Locate and identify every blood parasite.
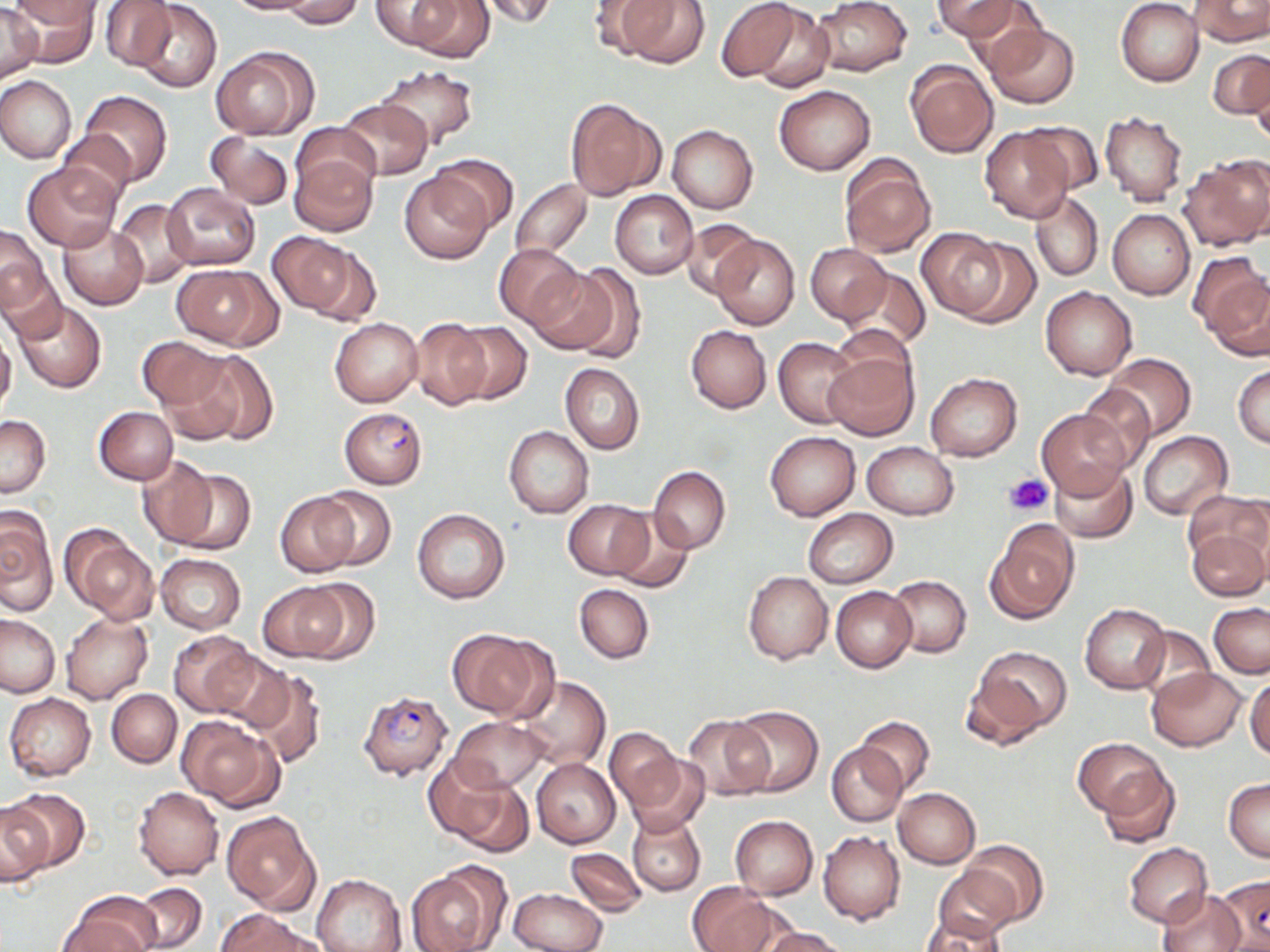

Approximate bounding boxes as (x1,y1)-(x2,y2) corner pairs in pixels.
Plasmodium falciparum-infected red blood cells: (338,407)-(428,489), (357,690)-(454,781), (1214,875)-(1270,951).
No Plasmodium ovale, Plasmodium malariae, Plasmodium vivax, Babesia divergens, or Trypanosoma brucei observed.

slide-level diagnosis = Plasmodium falciparum
magnification = 1000x
image size = 1270×952 pixels
field of view = single
preparation = thin blood film
uninfected red blood cell locations = approximate bounding boxes as (x1,y1)-(x2,y2) corner pairs in pixels: (8,0)-(102,52), (224,0)-(322,16), (280,0)-(366,29), (371,0)-(467,52), (474,0)-(561,27), (586,0)-(670,55), (618,0)-(710,69), (716,0)-(808,85), (812,0)-(911,77), (931,0)-(1026,43), (1116,0)-(1205,86), (1190,0)-(1269,46), (405,1)-(495,63), (100,2)-(176,70), (0,3)-(43,82), (135,3)-(221,91), (749,5)-(836,93), (983,22)-(1078,107), (210,47)-(318,139), (1209,48)-(1270,119), (905,59)-(998,157), (377,64)-(478,149), (0,76)-(76,163), (774,84)-(875,175), (78,90)-(171,186), (564,97)-(664,202), (338,99)-(432,180), (1099,110)-(1189,206), (1015,120)-(1104,196), (293,122)-(379,199), (667,124)-(759,214), (980,126)-(1074,223), (58,130)-(136,204), (205,131)-(294,210), (289,150)-(377,236), (430,154)-(519,233), (839,155)-(936,257), (1181,157)-(1270,252), (22,160)-(123,252), (400,171)-(495,263), (509,179)-(592,261), (162,183)-(260,271), (610,190)-(698,279), (1030,191)-(1104,281), (110,199)-(197,288), (1107,209)-(1195,300), (678,219)-(765,300), (58,224)-(149,309), (1,225)-(54,313), (916,228)-(1009,319), (266,232)-(360,317), (712,233)-(799,330), (950,237)-(1041,327), (302,243)-(384,327), (494,244)-(586,329), (805,245)-(892,324), (1192,253)-(1270,357), (478,257)-(571,368), (1,261)-(68,346), (566,262)-(649,363), (172,265)-(279,349), (838,266)-(931,351), (527,267)-(622,356), (1040,287)-(1137,381), (14,300)-(107,392), (331,318)-(424,407), (410,319)-(491,409), (447,321)-(531,404), (686,325)-(771,413), (0,331)-(16,413), (136,336)-(230,414), (773,337)-(861,429), (823,348)-(916,440), (177,349)-(277,447), (1103,353)-(1196,441), (561,363)-(645,454), (1233,364)-(1270,447), (926,372)-(1021,462), (1078,383)-(1157,474), (95,407)-(178,485), (1037,408)-(1130,501), (0,414)-(50,497), (504,426)-(594,518), (765,431)-(860,520), (1137,431)-(1232,519), (862,442)-(957,519), (136,456)-(220,547), (1050,461)-(1138,543), (648,467)-(730,554), (172,469)-(254,554), (312,487)-(397,571), (276,492)-(359,577), (563,499)-(652,580), (0,507)-(58,613), (412,508)-(509,604), (802,508)-(898,588), (608,510)-(696,592), (988,521)-(1078,622), (1185,522)-(1269,603), (63,529)-(157,622), (154,554)-(246,634), (743,570)-(833,665), (888,575)-(971,657), (298,581)-(379,662), (257,582)-(352,661), (575,583)-(654,664), (832,587)-(916,673), (1080,603)-(1171,694), (1209,603)-(1270,677), (0,613)-(59,697), (61,614)-(152,705), (1136,626)-(1215,702), (448,629)-(547,719), (168,630)-(259,717), (970,646)-(1072,741), (212,652)-(294,737), (1146,667)-(1246,751), (247,669)-(328,769), (1245,675)-(1270,762), (513,676)-(610,770), (107,689)-(181,767), (5,692)-(97,781), (730,706)-(822,795), (683,715)-(774,802), (177,716)-(281,809), (447,716)-(546,793), (855,716)-(935,795), (606,726)-(684,811), (1075,737)-(1169,821), (827,744)-(906,826), (628,754)-(709,835), (1095,756)-(1181,848), (531,758)-(620,848), (445,776)-(533,856), (1224,778)-(1270,862), (133,786)-(224,880), (893,787)-(981,867), (3,788)-(86,875), (0,800)-(49,886), (626,809)-(706,897), (221,811)-(320,914), (729,815)-(818,899), (818,831)-(905,925), (960,839)-(1048,927), (1124,843)-(1213,927), (566,848)-(646,916), (933,865)-(1023,943), (406,867)-(499,952), (312,874)-(406,952), (133,883)-(206,950), (687,883)-(780,952), (510,888)-(606,952), (1155,888)-(1246,952), (59,893)-(159,952), (215,911)-(315,952), (919,918)-(1011,952), (759,927)-(847,952)
platelet locations = approximate bounding boxes as (x1,y1)-(x2,y2) corner pairs in pixels: (1004,473)-(1052,514)
stain = May-Grünwald-Giemsa
modality = light microscopy